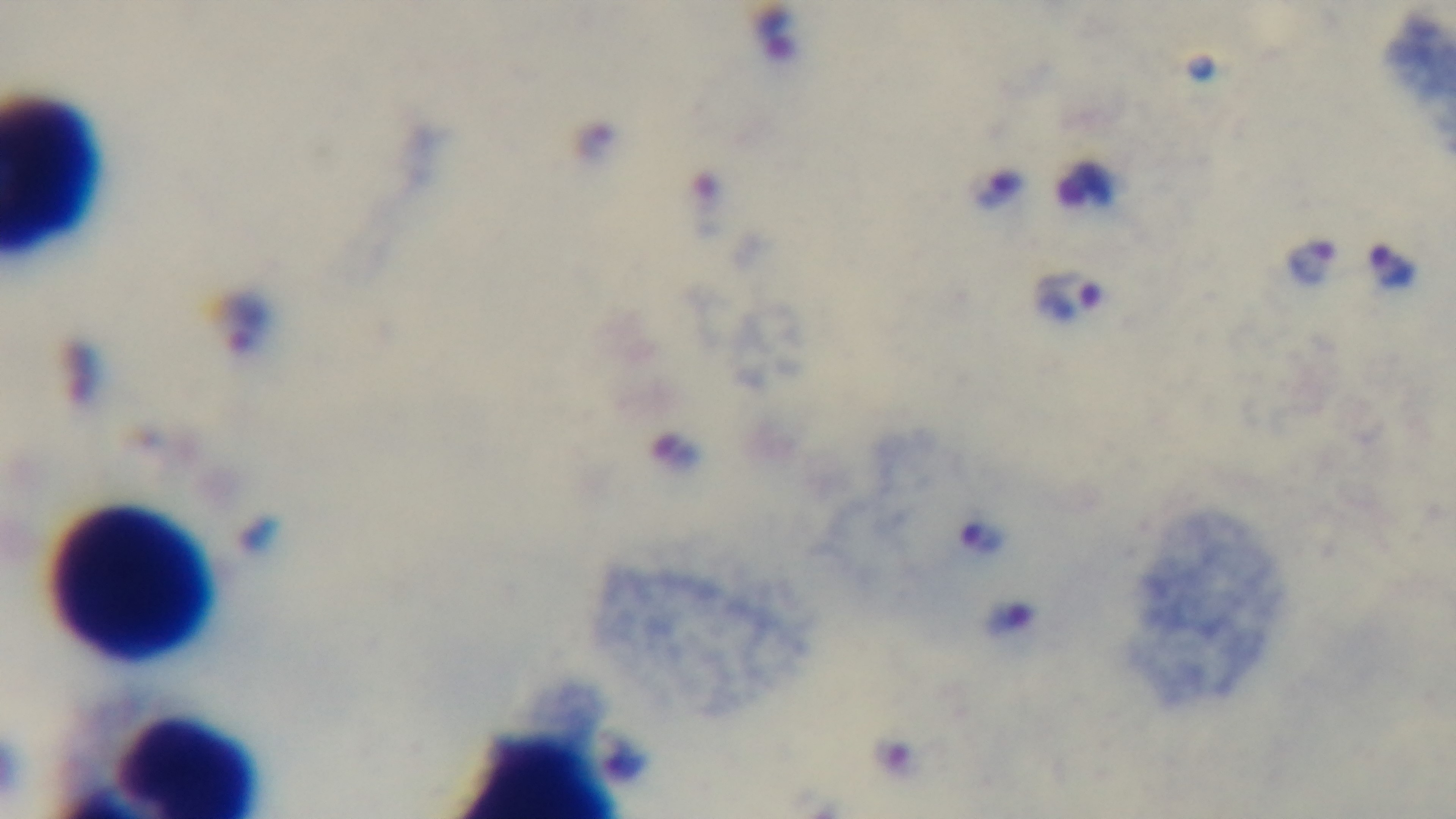

capture: mounted 4K digital camera
preparation: thick blood film
modality: light microscopy
malaria_status: infected
field_of_view: single
objective: 100x oil immersion
stain: Giemsa